Name the parasite shown.
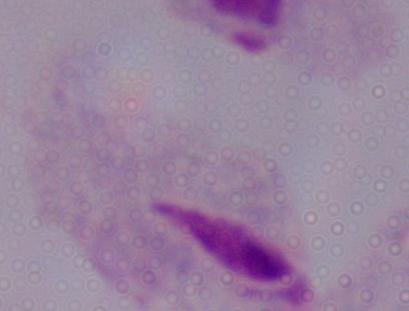
This is a trichomonad.

Summary:
  - Modality: photomicrograph
  - Magnification: 1000x